Describe the morphology of the erythrocytes.
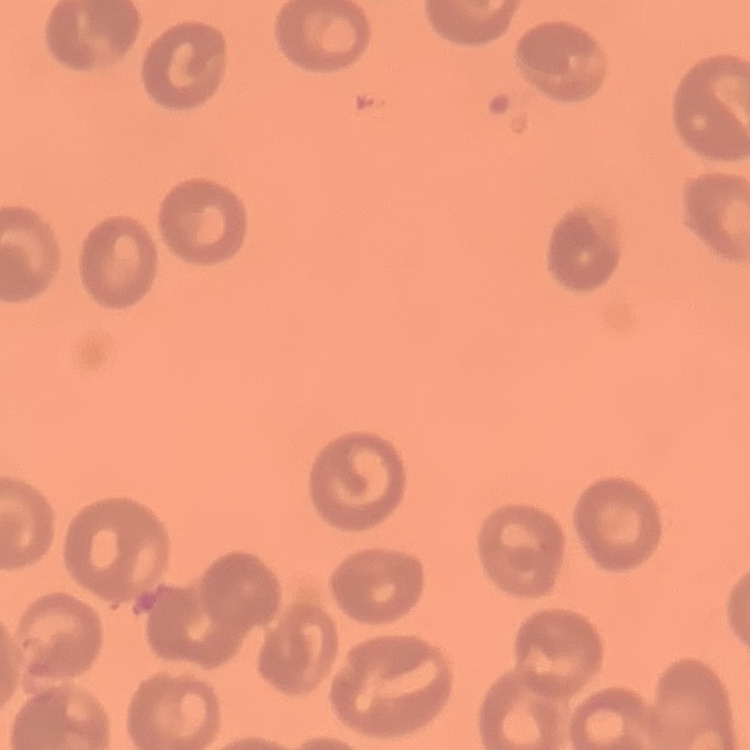

No rouleaux formation.

Square crop of a larger photomicrograph. Field's or Giemsa stain. Thin peripheral smear.